Assess this cell for malaria.
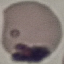

It is uninfected.

Summary:
  - Capture: smartphone camera at the microscope eyepiece
  - Image type: automatically extracted cell patch, resized to 64 × 64 pixels
  - Preparation: thin smear
  - Stain: Giemsa